State the preparation type.
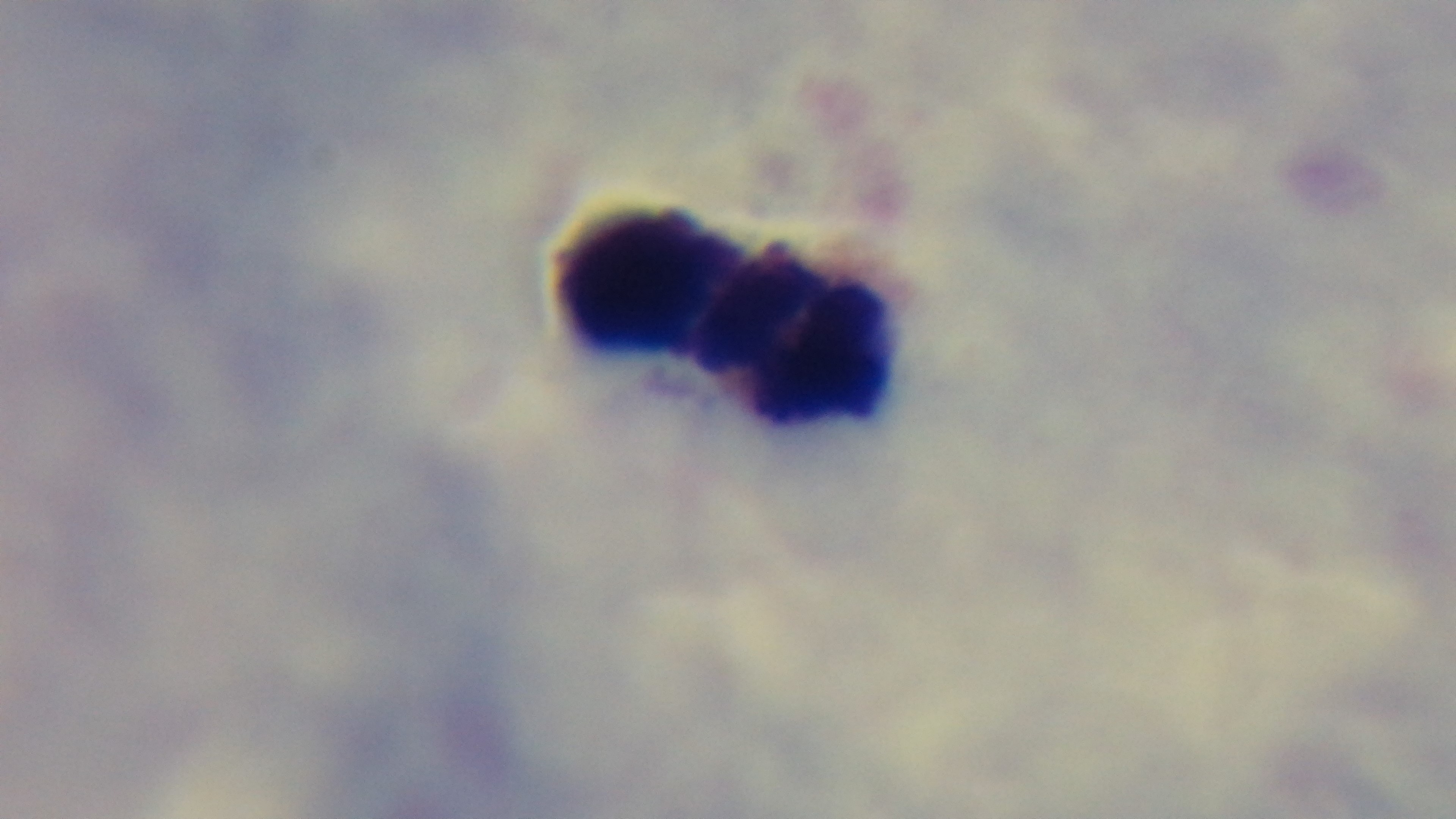
It is a thick blood film.

{
  "modality": "light microscopy",
  "malaria_status": "negative",
  "capture": "mounted 4K digital camera",
  "field_of_view": "one from the slide",
  "objective": "100x oil immersion",
  "stain": "Giemsa"
}